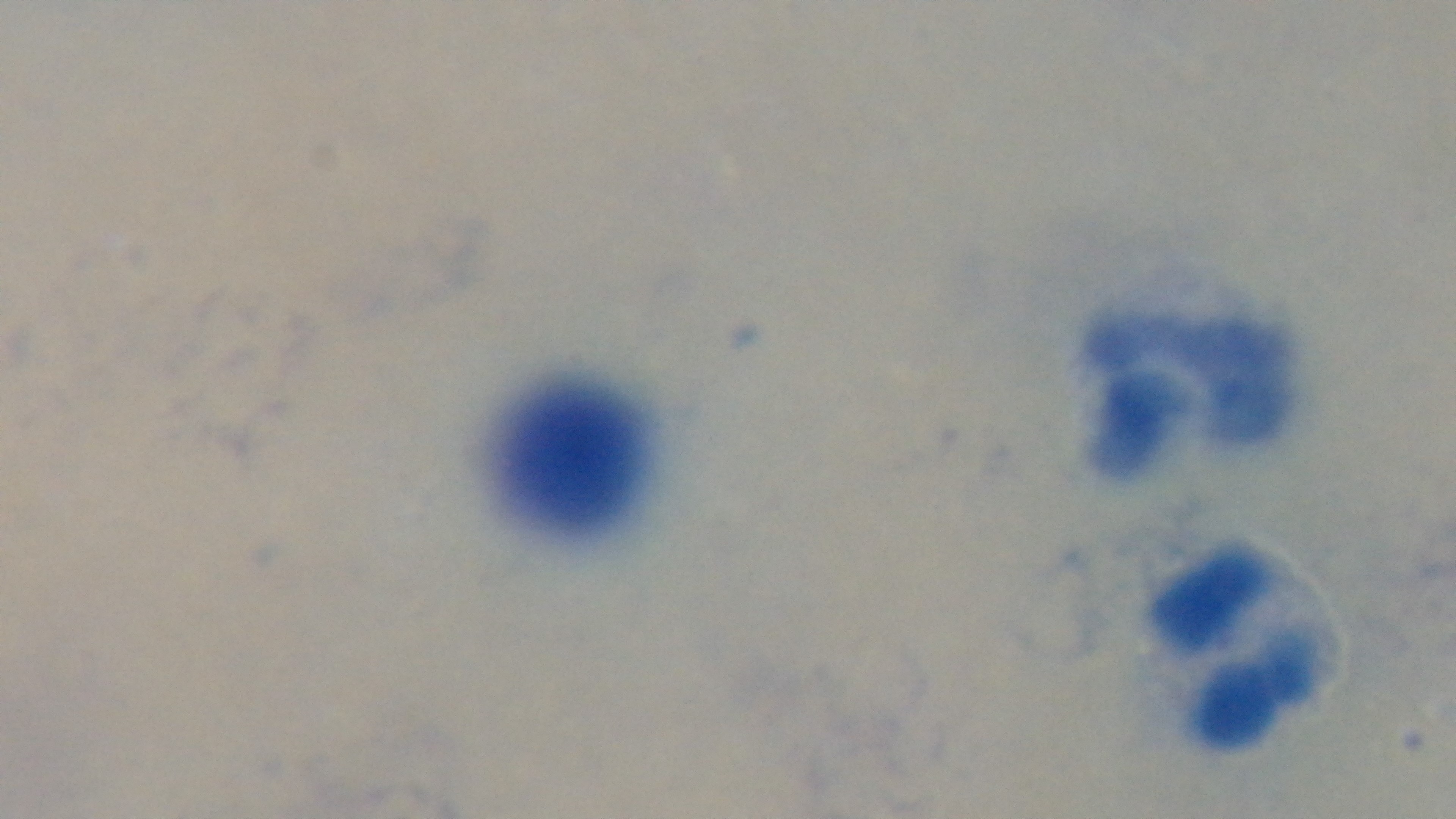 Single field of view. Mounted 4K digital camera. Malaria status: negative. Preparation: thick blood film. Oil-immersion objective, 100x. Giemsa stain. Light microscopy.